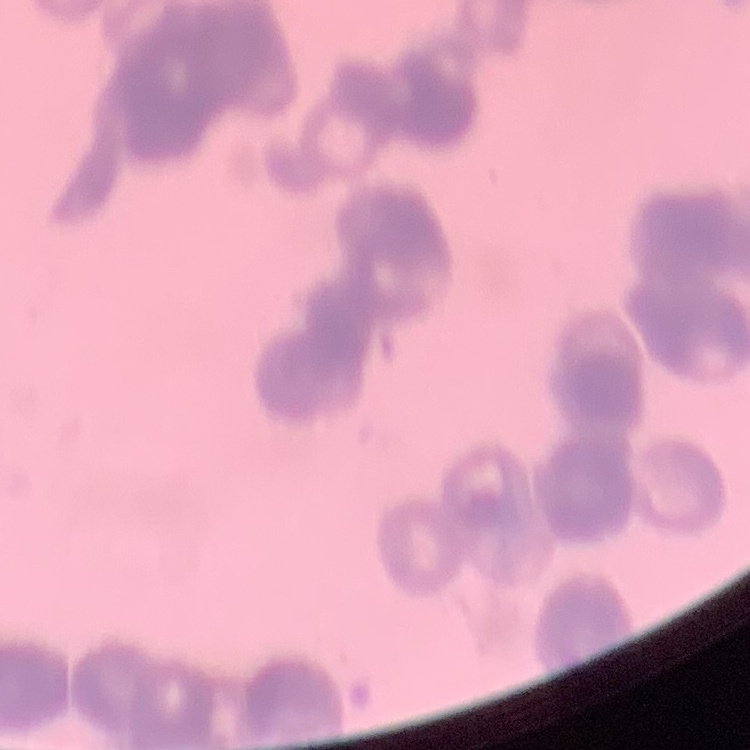
Summary:
  - Erythrocyte morphology: rouleaux formation
  - Image type: one tile cut from a larger photomicrograph
  - Stain: Field's or Giemsa
  - Preparation: thin peripheral smear